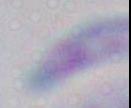
Captured at 1000x magnification. Toxoplasma gondii is seen. Photomicrograph.